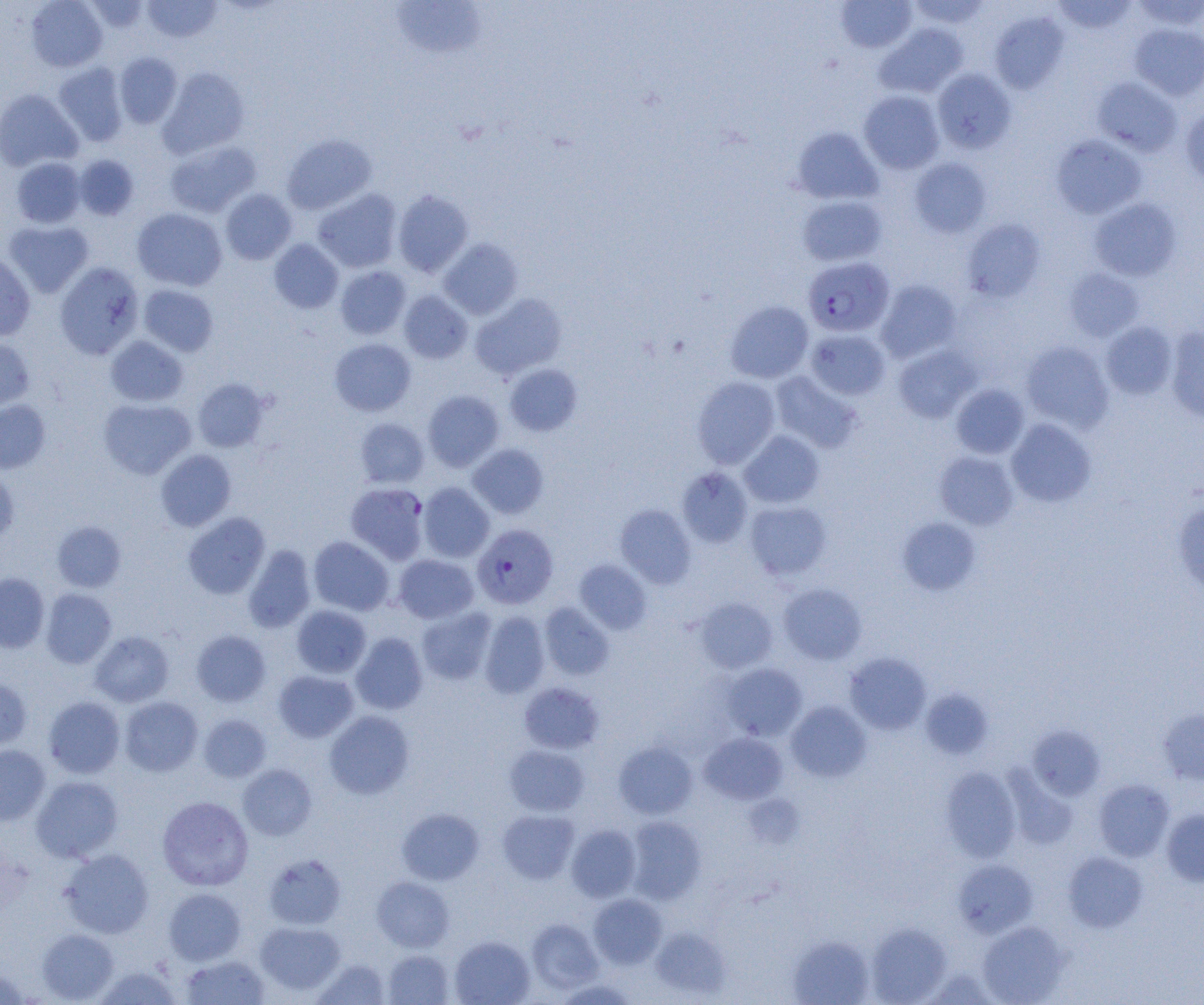

slide-level diagnosis = Plasmodium falciparum
image size = 1204×1005 pixels
field of view = single
modality = light microscopy
uninfected red blood cell locations = approximate bounding boxes as [x1, y1, x2, y2] in pixels: [26, 0, 107, 72], [142, 0, 222, 43], [907, 0, 991, 29], [1052, 0, 1137, 36], [1130, 0, 1204, 31], [83, 1, 150, 32], [390, 1, 487, 58], [836, 1, 916, 52], [990, 11, 1069, 93], [875, 23, 968, 98], [1130, 23, 1204, 100], [114, 52, 182, 128], [53, 62, 128, 146], [158, 67, 250, 159], [932, 68, 1016, 154], [1091, 76, 1183, 157], [0, 89, 82, 172], [859, 90, 945, 174], [1180, 106, 1204, 187], [792, 127, 883, 205], [281, 134, 376, 215], [1051, 134, 1147, 219], [165, 140, 261, 217], [74, 155, 139, 220], [11, 157, 87, 228], [909, 157, 992, 238], [220, 189, 297, 264], [313, 189, 402, 273], [393, 190, 474, 277], [797, 195, 887, 267], [1089, 197, 1182, 281], [132, 208, 227, 291], [961, 219, 1044, 302], [3, 220, 94, 298], [439, 238, 523, 319], [269, 239, 343, 313], [0, 251, 35, 341], [55, 262, 144, 359], [335, 266, 411, 340], [1064, 268, 1144, 342], [876, 280, 961, 363], [138, 284, 218, 356], [399, 291, 472, 363], [470, 293, 567, 380], [725, 301, 813, 383], [1101, 321, 1178, 399], [1165, 327, 1204, 422], [805, 329, 890, 400], [0, 336, 35, 410], [105, 336, 188, 407], [329, 338, 416, 416], [1020, 341, 1113, 432], [893, 344, 981, 423], [504, 363, 583, 437], [770, 372, 862, 453], [692, 376, 781, 469], [193, 378, 270, 452], [951, 384, 1029, 459], [422, 390, 504, 472], [98, 398, 196, 479], [0, 399, 51, 474], [355, 418, 429, 488], [1006, 419, 1096, 507], [739, 430, 824, 508], [468, 444, 549, 518], [156, 449, 236, 531], [934, 451, 1019, 530], [677, 467, 753, 548], [0, 468, 19, 547], [345, 482, 429, 565], [418, 482, 494, 562], [745, 501, 832, 580], [1173, 501, 1204, 596], [615, 504, 697, 588], [183, 512, 269, 598], [897, 516, 981, 595], [52, 521, 126, 592], [308, 536, 394, 616], [243, 545, 316, 633], [393, 554, 479, 623], [574, 560, 651, 634], [0, 573, 49, 653], [778, 583, 867, 664], [41, 589, 117, 668], [693, 597, 777, 674], [539, 603, 614, 680], [291, 605, 371, 678], [416, 607, 496, 685], [479, 611, 550, 698], [192, 630, 271, 706], [89, 631, 174, 707], [350, 632, 428, 715], [844, 652, 931, 735], [722, 662, 807, 741], [273, 670, 358, 743], [0, 676, 32, 750], [518, 682, 604, 754], [921, 689, 992, 760], [43, 696, 125, 778], [120, 696, 203, 776], [786, 701, 871, 782], [1158, 708, 1204, 785], [325, 710, 415, 799], [199, 714, 271, 782], [1027, 725, 1105, 801], [700, 732, 787, 805], [614, 741, 697, 819], [504, 744, 589, 816], [0, 745, 50, 825], [237, 764, 317, 841], [940, 767, 1021, 861], [1004, 770, 1079, 850], [31, 775, 123, 862], [1093, 779, 1174, 861], [157, 796, 253, 891], [397, 808, 484, 885], [497, 809, 579, 884], [1162, 809, 1204, 886], [625, 816, 707, 904], [566, 824, 641, 902], [60, 848, 154, 938], [1063, 851, 1147, 932], [263, 853, 347, 930], [953, 859, 1038, 937], [372, 876, 454, 952], [163, 888, 246, 965], [588, 893, 666, 969], [527, 918, 603, 993], [255, 921, 346, 995], [978, 921, 1068, 1005], [866, 923, 951, 1004], [650, 927, 730, 998], [37, 928, 119, 1003], [450, 936, 534, 1005], [788, 936, 874, 1005], [384, 950, 454, 1005], [181, 955, 270, 1005], [311, 958, 391, 1004], [94, 965, 182, 1005], [0, 967, 30, 1005], [553, 978, 640, 1005]
preparation = thin blood smear
Plasmodium falciparum-infected red blood cell locations = approximate bounding boxes as [x1, y1, x2, y2] in pixels: [802, 256, 894, 337], [472, 524, 558, 609]
magnification = 1000x